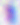
modality = micrograph
magnification = 400x
identification = Toxoplasma gondii